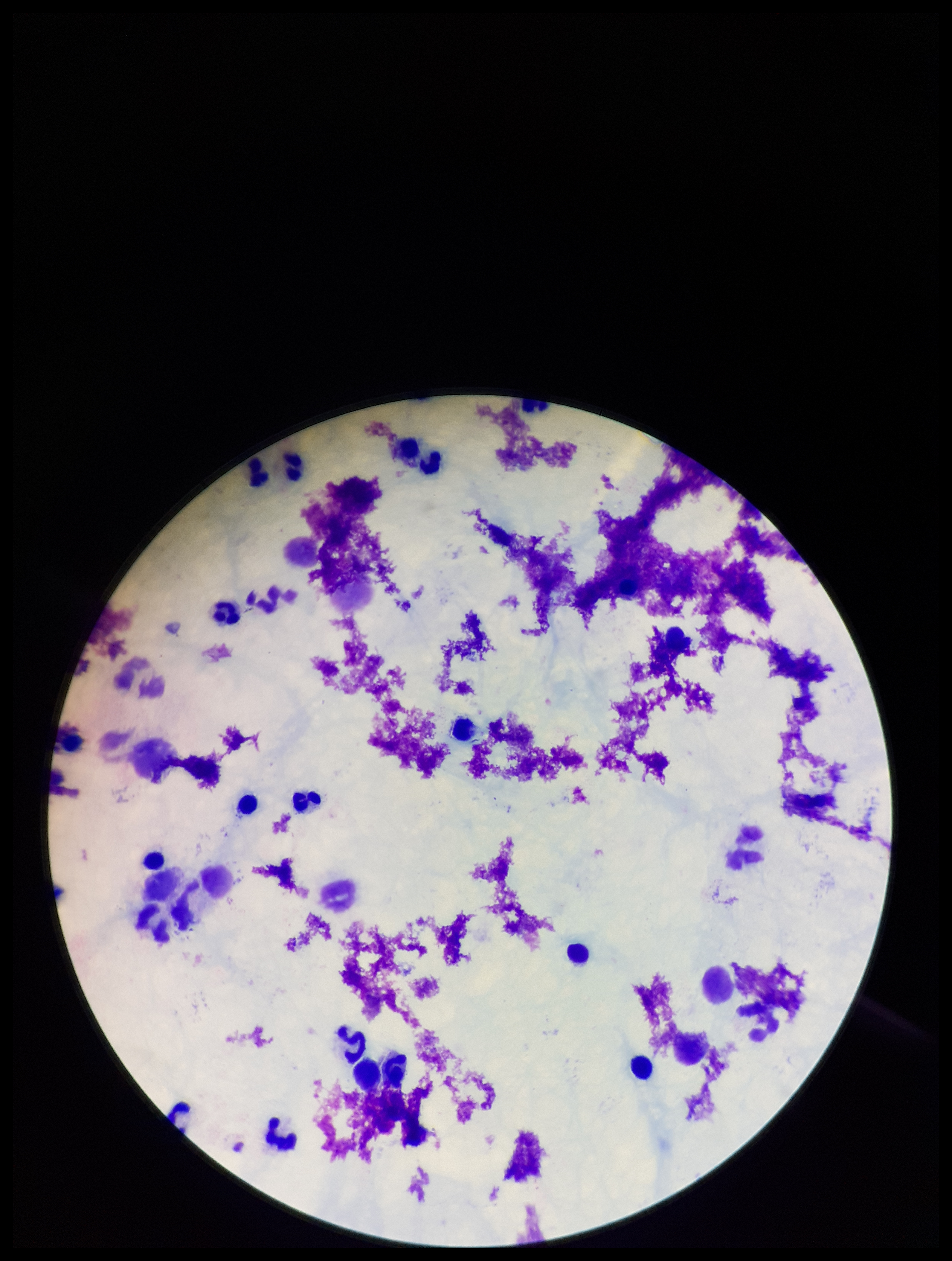

capture = smartphone photograph through the microscope eyepiece
parasite count = 0
leukocyte count = 22
stain = Giemsa
patient malaria status = negative
Plasmodium parasites = none detected
field of view = one from this slide
image size = 952×1261 pixels
preparation = thick blood smear